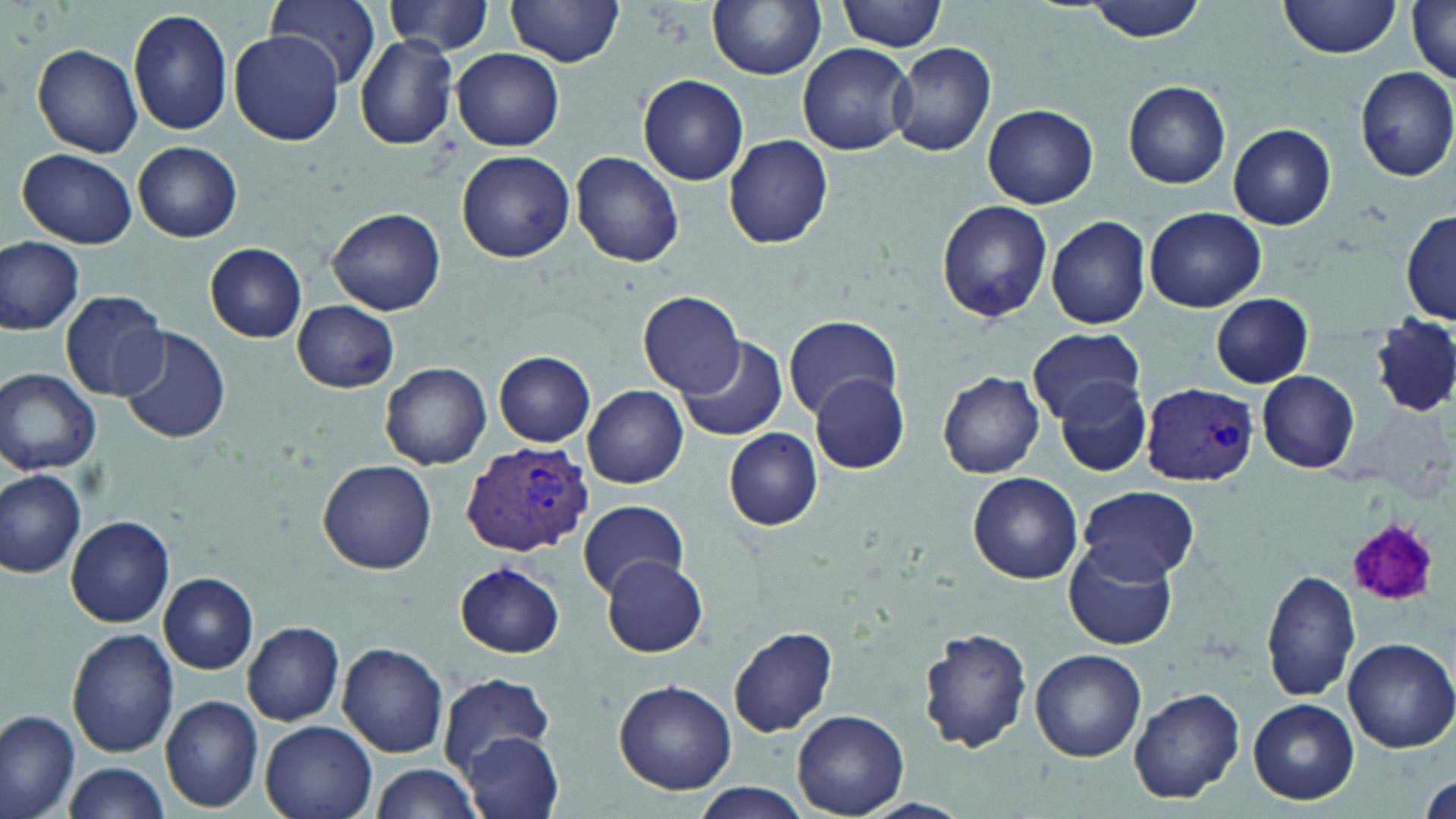

Approximate bounding boxes as [x1, y1, x2, y2] in pixels. Platelet locations: [1344, 516, 1443, 608]. Plasmodium vivax-infected red blood cell locations: [1143, 382, 1259, 485], [460, 441, 592, 557]. Uninfected red blood cell locations: [262, 0, 382, 90], [708, 0, 827, 80], [837, 0, 947, 52], [1082, 0, 1209, 42], [1280, 0, 1401, 58], [507, 1, 624, 68], [384, 2, 495, 54], [1406, 2, 1456, 83], [126, 7, 233, 136], [230, 31, 342, 146], [352, 35, 459, 151], [889, 41, 997, 157], [31, 43, 143, 157], [798, 43, 914, 155], [452, 48, 565, 151], [1355, 67, 1456, 182], [637, 74, 749, 185], [1124, 80, 1231, 190], [983, 104, 1098, 208], [1229, 124, 1335, 230], [725, 135, 832, 249], [134, 142, 242, 241], [17, 149, 139, 249], [458, 150, 574, 262], [571, 151, 683, 269], [936, 200, 1053, 322], [1145, 207, 1265, 312], [328, 208, 446, 315], [1401, 212, 1455, 325], [1045, 216, 1153, 329], [0, 235, 83, 335], [205, 242, 308, 343], [61, 290, 170, 400], [636, 290, 746, 399], [1209, 295, 1314, 386], [291, 300, 401, 392], [783, 314, 899, 419], [1370, 316, 1455, 418], [117, 325, 230, 443], [1026, 328, 1147, 424], [676, 336, 787, 441], [495, 351, 594, 446], [379, 361, 492, 469], [1, 368, 101, 475], [938, 369, 1045, 479], [1257, 371, 1359, 473], [810, 373, 910, 475], [1055, 376, 1153, 477], [583, 384, 688, 488], [723, 427, 823, 531], [317, 461, 436, 574], [0, 469, 87, 578], [967, 472, 1083, 585], [1076, 485, 1199, 583], [577, 499, 687, 598], [66, 514, 174, 628], [1065, 542, 1176, 651], [602, 557, 707, 657], [456, 561, 564, 658], [1261, 568, 1359, 703], [159, 573, 258, 673], [243, 622, 344, 724], [729, 625, 838, 737], [67, 627, 178, 758], [917, 628, 1032, 754], [1342, 638, 1456, 753], [337, 642, 448, 758], [1030, 648, 1145, 761], [438, 673, 554, 771], [615, 681, 736, 794], [1129, 687, 1246, 804], [160, 695, 263, 811], [1248, 698, 1359, 804], [0, 708, 81, 817], [791, 710, 909, 816], [260, 719, 377, 819], [462, 731, 566, 819], [62, 761, 173, 816], [365, 764, 483, 819], [691, 783, 812, 816]. Slide-level diagnosis: Plasmodium vivax. Captured at 1000x magnification. Light microscopy. Image is 1456×819 pixels. One field of a larger specimen. May-Grünwald-Giemsa stain. Thin blood smear.